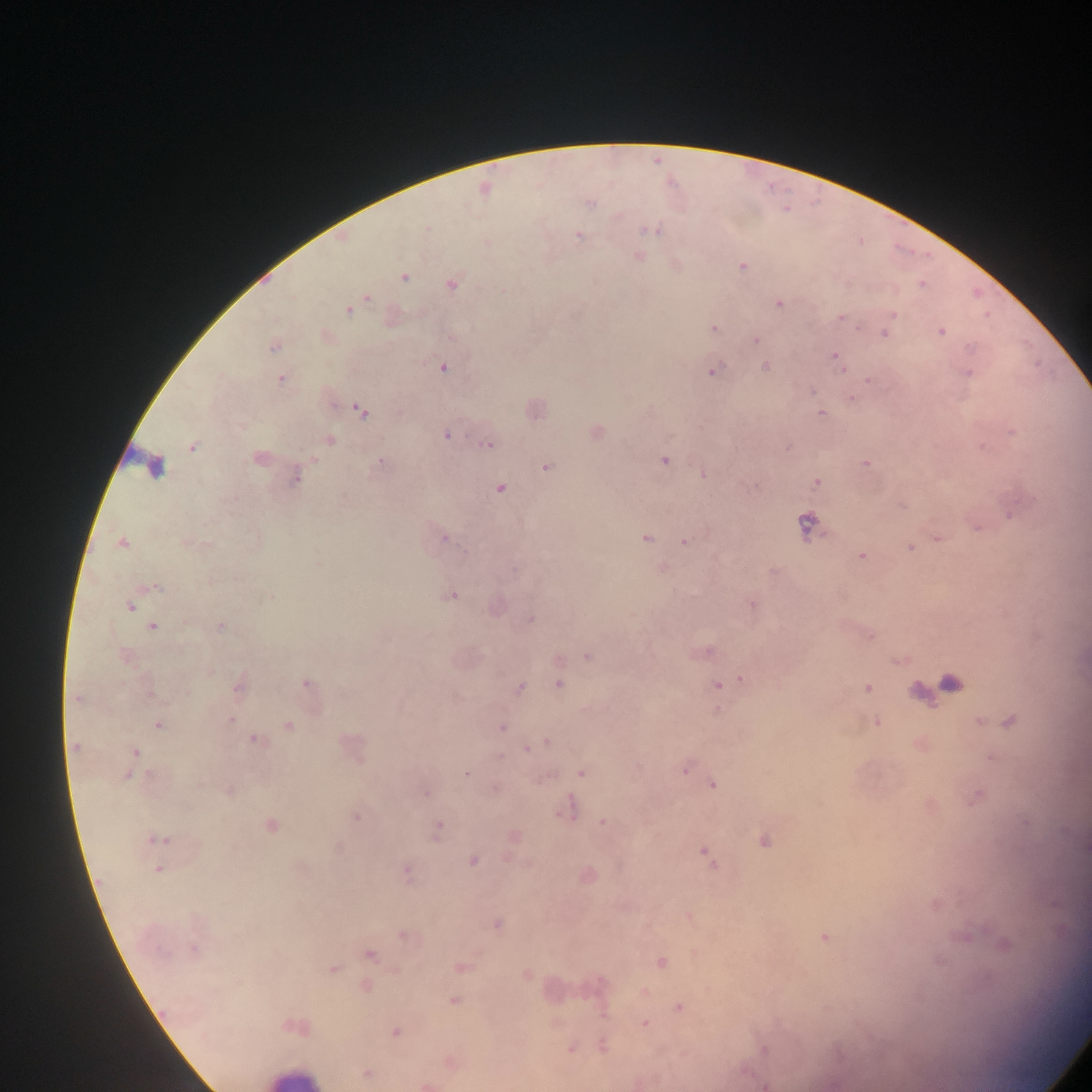 Approximate centers as {x, y} in pixels. Leukocyte locations: {294, 1077}. Plasmodium parasite locations: {592, 202}, {659, 228}, {642, 229}, {652, 230}, {577, 235}, {638, 255}, {742, 265}, {405, 277}, {452, 284}, {921, 284}, {502, 290}, {366, 297}, {779, 304}, {348, 310}, {893, 314}, {841, 317}, {713, 327}, {858, 328}, {940, 332}, {882, 333}, {755, 340}, {969, 346}, {274, 348}, {834, 356}, {765, 366}, {444, 367}, {841, 370}, {712, 371}, {968, 373}, {280, 378}, {867, 379}, {811, 390}, {851, 398}, {359, 408}, {821, 413}, {241, 427}, {1010, 431}, {446, 434}, {330, 439}, {487, 443}, {787, 446}, {982, 446}, {192, 447}, {257, 457}, {664, 460}, {313, 461}, {379, 461}, {865, 462}, {153, 466}, {546, 468}, {703, 474}, {295, 476}, {816, 482}, {755, 485}, {499, 487}, {1007, 512}, {808, 524}, {976, 527}, {647, 538}, {936, 538}, {443, 539}, {123, 542}, {684, 542}, {207, 544}, {909, 548}, {862, 555}, {774, 570}, {155, 586}, {454, 594}, {753, 604}, {131, 607}, {530, 619}, {154, 626}, {221, 626}, {870, 636}, {702, 653}, {587, 657}, {897, 662}, {741, 678}, {306, 682}, {950, 682}, {559, 685}, {717, 686}, {520, 688}, {867, 688}, {915, 688}, {238, 690}, {151, 692}, {187, 692}, {74, 699}, {231, 720}, {979, 721}, {877, 722}, {1009, 722}, {160, 726}, {290, 726}, {502, 727}, {257, 741}, {545, 741}, {539, 745}, {74, 746}, {527, 747}, {136, 752}, {500, 757}, {356, 758}, {989, 758}, {685, 770}, {580, 772}, {128, 773}, {466, 773}, {149, 774}, {543, 778}, {713, 784}, {201, 785}, {229, 790}, {425, 794}, {978, 797}, {574, 808}, {565, 810}, {558, 813}, {358, 815}, {601, 822}, {271, 826}, {437, 826}, {514, 836}, {150, 839}, {167, 840}, {763, 840}, {154, 841}, {704, 854}, {511, 859}, {473, 860}, {524, 860}, {529, 863}, {712, 863}, {159, 869}, {406, 871}, {687, 916}, {496, 924}, {404, 936}, {823, 936}, {193, 949}, {166, 951}, {371, 955}, {660, 963}, {460, 967}, {332, 968}, {395, 970}, {527, 974}, {988, 976}, {365, 985}, {454, 1001}, {678, 1007}, {824, 1008}, {645, 1023}, {286, 1027}, {397, 1031}, {570, 1048}, {764, 1051}, {366, 1073}, {427, 1085}, {764, 1085}. Image is 1092×1092 pixels. Mobile-phone photograph taken through the microscope. One field of view. Thick blood smear. Collected in Ghana.